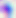
modality = photomicrograph
identification = Toxoplasma gondii
magnification = 400x